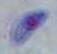 Toxoplasma gondii is seen. Captured at 1000x magnification. Photomicrograph.